Identify the preparation type.
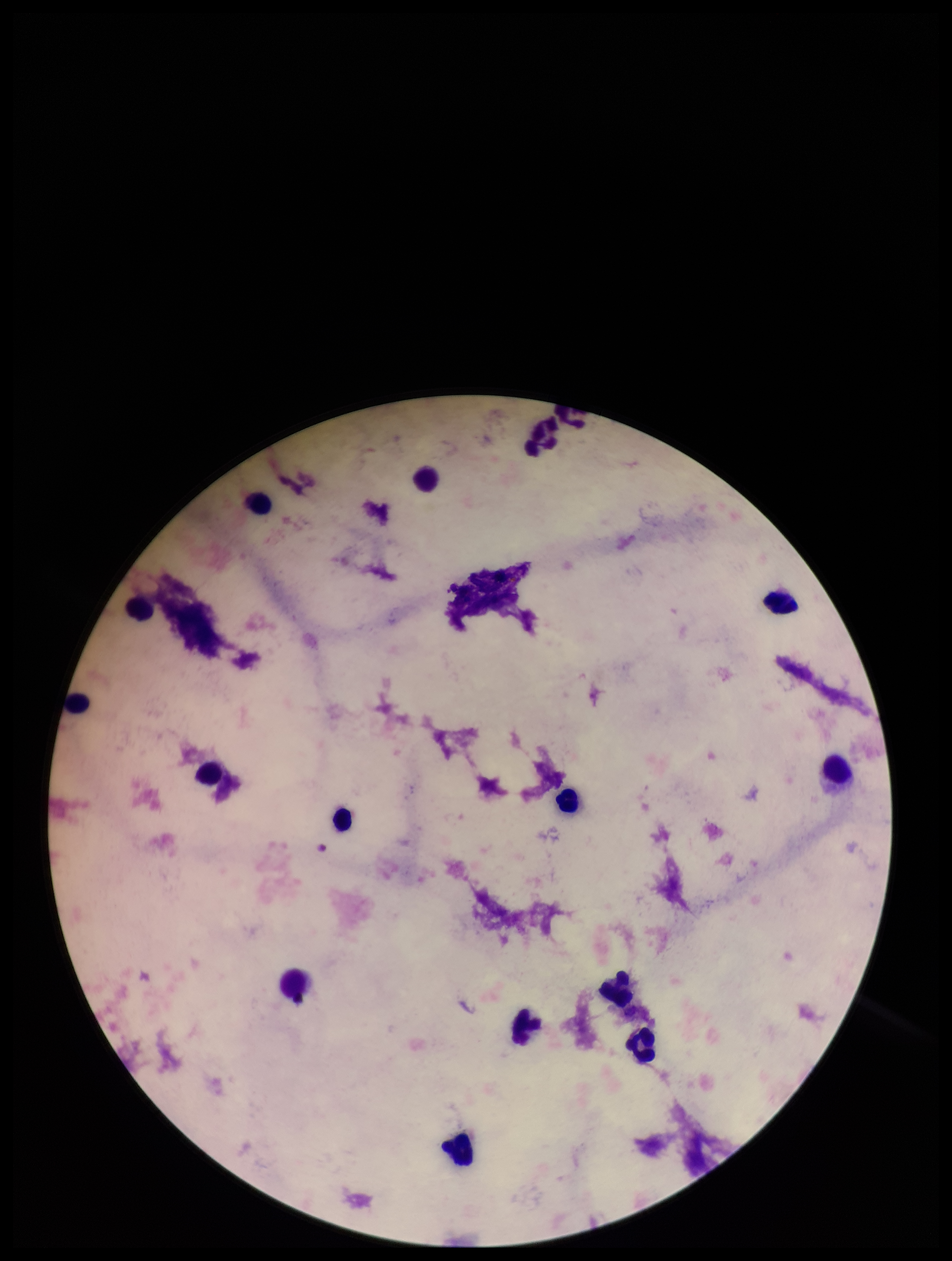
It is a thick blood smear.

Image is 952×1261 pixels. Parasite count: 0. Patient malaria status: negative. Single field of view. Plasmodium parasites: none identified. Leukocyte count: 15. Stained with Giemsa. Photographed through the microscope eyepiece with a smartphone camera.